Report the malaria status of this cell.
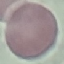

It is uninfected.

image type = cell patch, automatically extracted from a larger field of view and resized to 64 × 64 pixels
preparation = thin blood film
stain = Giemsa
capture = smartphone through the microscope eyepiece